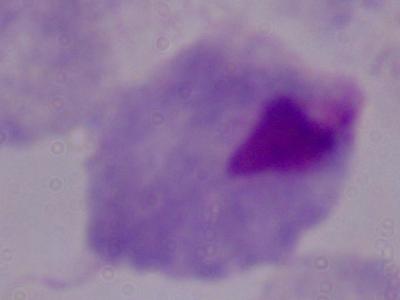
Summary:
  - Magnification: 1000x
  - Identification: trichomonad
  - Modality: photomicrograph